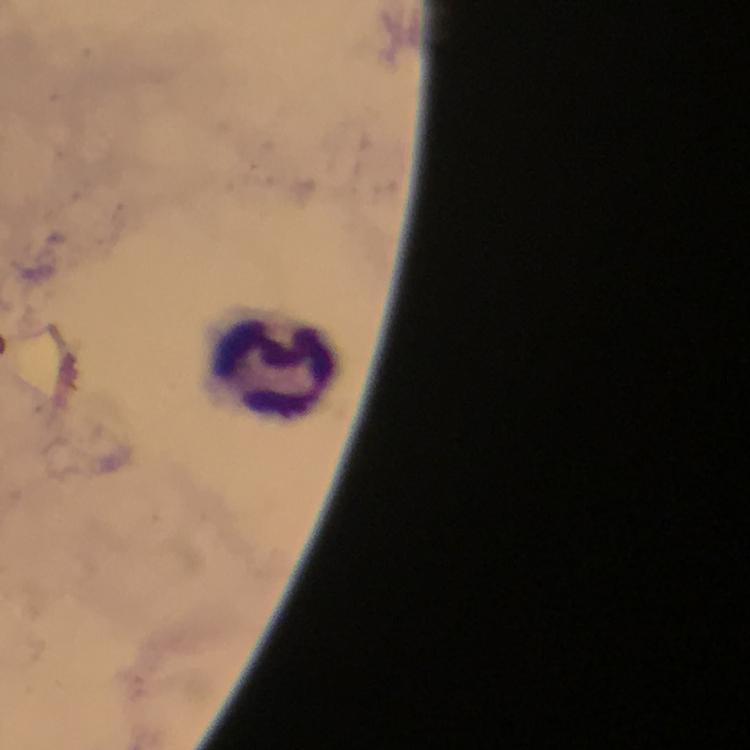 Approximate centers as (x, y) in pixels. Leukocyte locations: (272, 368). Smartphone photograph taken through a microscope. At 100x magnification. Giemsa-stained preparation. Thick blood smear. Immersion oil was used. Image is 750×750 pixels. From a diagnostic examination for malaria. Cropped region of a single field of view. Malaria parasites: none seen.